Evaluate for Plasmodium parasites.
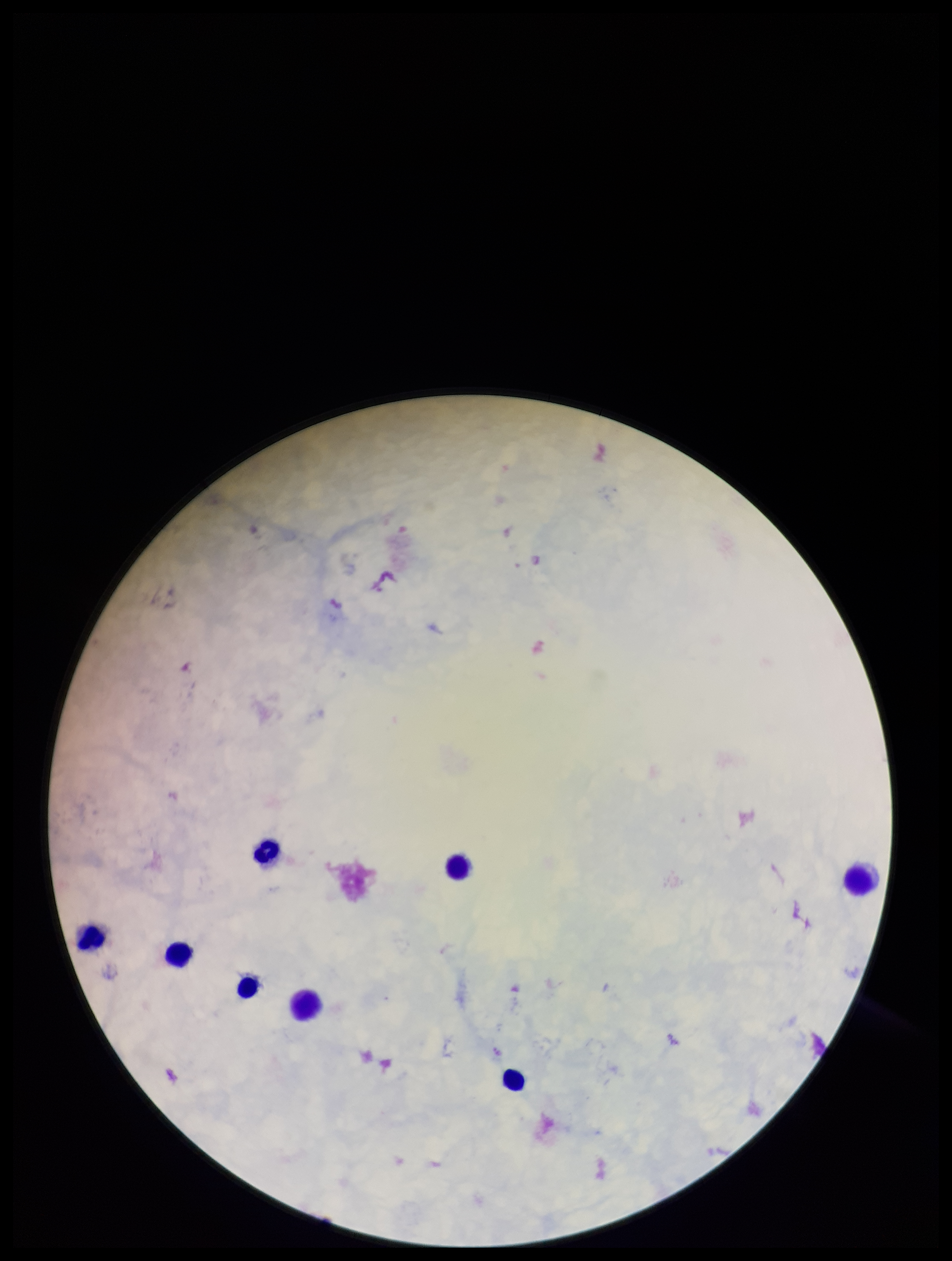

None detected.

parasite count = 0
leukocyte count = 8
stain = Giemsa
image size = 952×1261 pixels
patient malaria status = negative
capture = smartphone photograph through the microscope eyepiece
preparation = thick blood smear
field of view = single